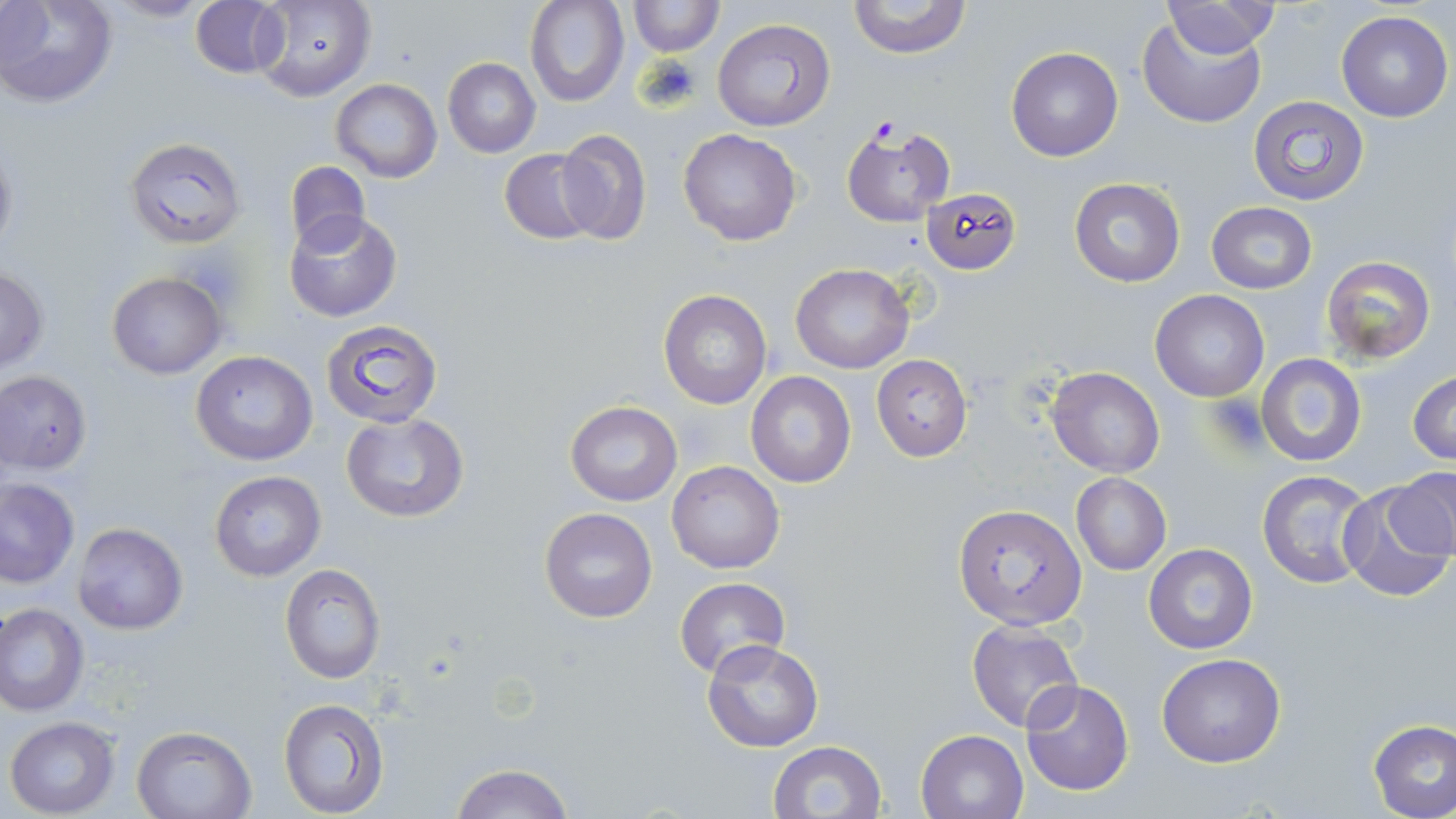

Summary:
  - Coordinate format: approximate bounding boxes as (x1,y1)-(x2,y2) corner pairs in pixels
  - Uninfected red blood cell locations: (0,0)-(118,109), (524,0)-(628,107), (626,0)-(723,56), (252,1)-(376,102), (847,1)-(972,59), (1160,1)-(1277,60), (189,2)-(289,78), (1336,11)-(1453,122), (1138,14)-(1265,129), (711,18)-(835,131), (1006,47)-(1123,161), (442,57)-(541,157), (330,79)-(442,183), (1246,94)-(1370,208), (677,129)-(802,245), (553,130)-(652,243), (123,137)-(248,250), (498,147)-(599,245), (285,161)-(370,253), (1069,177)-(1186,288), (921,186)-(1021,274), (1205,202)-(1317,294), (284,208)-(401,321), (1321,255)-(1436,363), (791,263)-(914,374), (0,267)-(48,373), (107,271)-(226,380), (658,289)-(772,410), (1149,289)-(1269,403), (323,318)-(444,428), (192,351)-(319,465), (1255,353)-(1367,466), (871,355)-(973,461), (1045,366)-(1165,477), (0,370)-(93,474), (1408,370)-(1456,464), (746,371)-(856,488), (566,401)-(682,507), (342,413)-(469,523), (668,461)-(786,572), (1257,468)-(1377,591), (1389,468)-(1456,565), (209,469)-(326,582), (1070,473)-(1172,575), (1,478)-(78,587), (1340,486)-(1452,602), (953,503)-(1086,632), (539,507)-(658,623), (73,523)-(189,635), (1144,543)-(1258,655), (279,563)-(386,684), (673,577)-(790,679), (0,603)-(89,716), (966,621)-(1083,734), (701,641)-(823,752), (1157,653)-(1286,768), (1020,678)-(1135,796), (278,697)-(389,817), (5,716)-(120,817), (1368,719)-(1456,818), (130,723)-(257,819), (915,728)-(1027,819), (768,740)-(888,819), (450,762)-(574,819)
  - Plasmodium falciparum-infected red blood cell locations: (840,123)-(957,227)
  - Platelet locations: (637,53)-(703,112)
  - Slide-level diagnosis: Plasmodium falciparum
  - Field of view: one of a larger specimen
  - Stain: May-Grünwald-Giemsa
  - Preparation: thin blood film
  - Magnification: 1000x
  - Image size: 1456×819 pixels
  - Modality: light microscopy